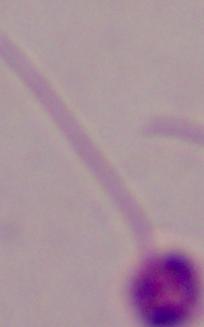

Summary:
  - Modality: photomicrograph
  - Magnification: 1000x
  - Identification: Leishmania